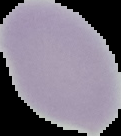

{
  "malaria_status": "uninfected",
  "image_type": "segmented cell region on a black background",
  "preparation": "thin blood film",
  "image_size": "121×136 pixels"
}